Assess the morphology of the erythrocytes.
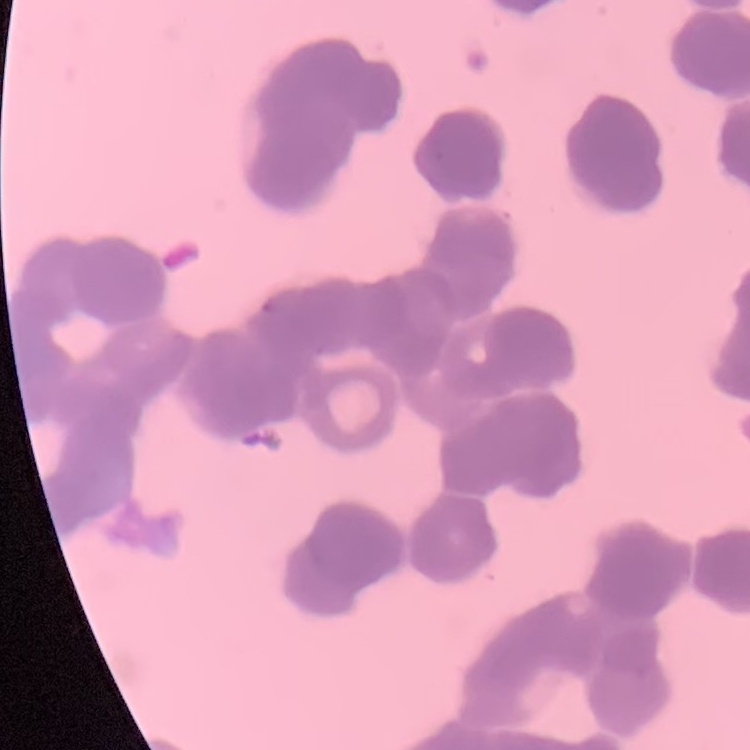
Rouleaux formation.

Thin blood film. Field's or Giemsa stain. One tile cut from a larger photomicrograph.